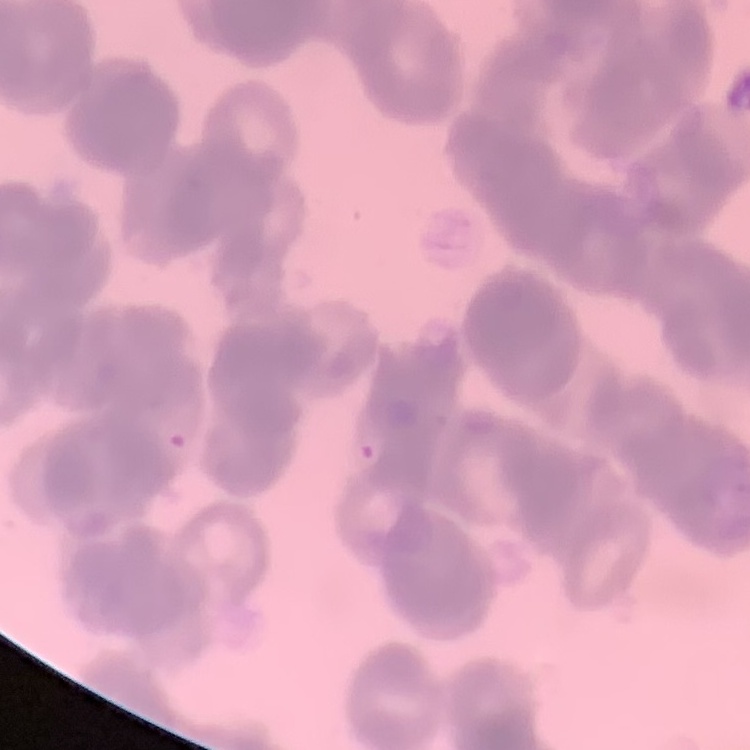 The red blood cells exhibit rouleaux formation. Field's or Giemsa stain. Square crop of a larger photomicrograph. Thin blood smear.